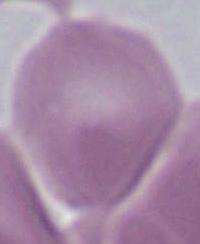
magnification = 1000x
modality = micrograph
identification = red blood cell